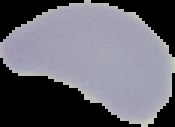
Summary:
  - Preparation: thin blood film
  - Image type: cell region segmented out of the field of view; surrounding area masked to black
  - Result: no Plasmodium parasites detected
  - Image size: 175×127 pixels